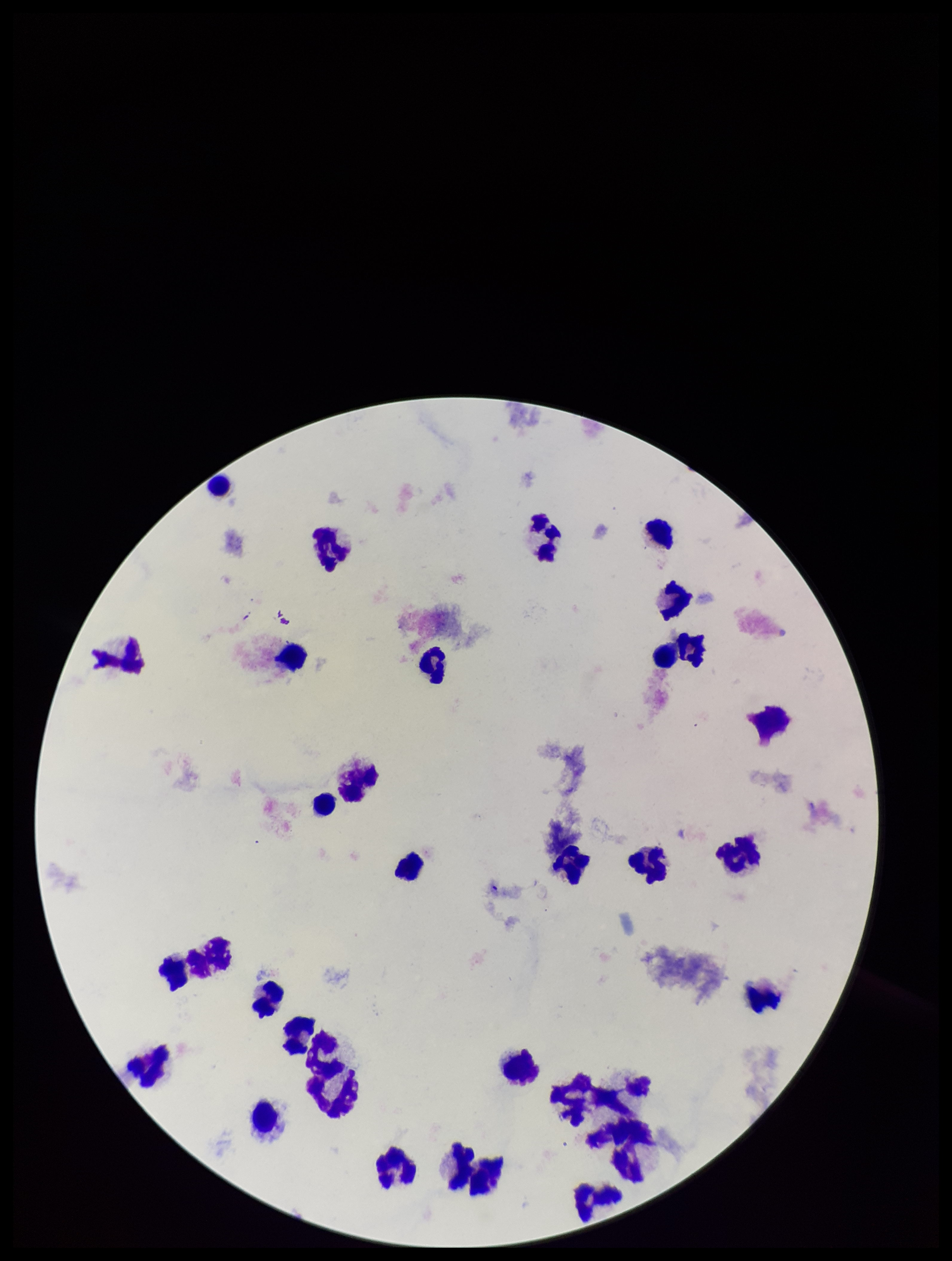
Summary:
  - Patient malaria status: negative
  - Preparation: thick blood smear
  - Stain: Giemsa
  - Image size: 952×1261 pixels
  - Parasite count: 0
  - Leukocyte count: 29
  - Field of view: single
  - Plasmodium parasites: none detected
  - Capture: smartphone photograph through the microscope eyepiece